Classify this cell by malaria status.
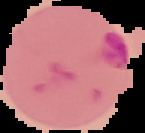

It is parasitized.

Segmented cell region on a black background. From a thin blood smear. Image is 145×133 pixels.